Assess this cell for malaria.
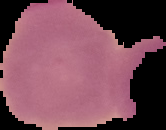

Uninfected.

Segmented cell region on a black background. Image is 166×130 pixels. From a thin blood film.